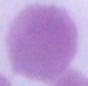

Summary:
  - Magnification: 1000x
  - Modality: micrograph
  - Identification: red blood cell